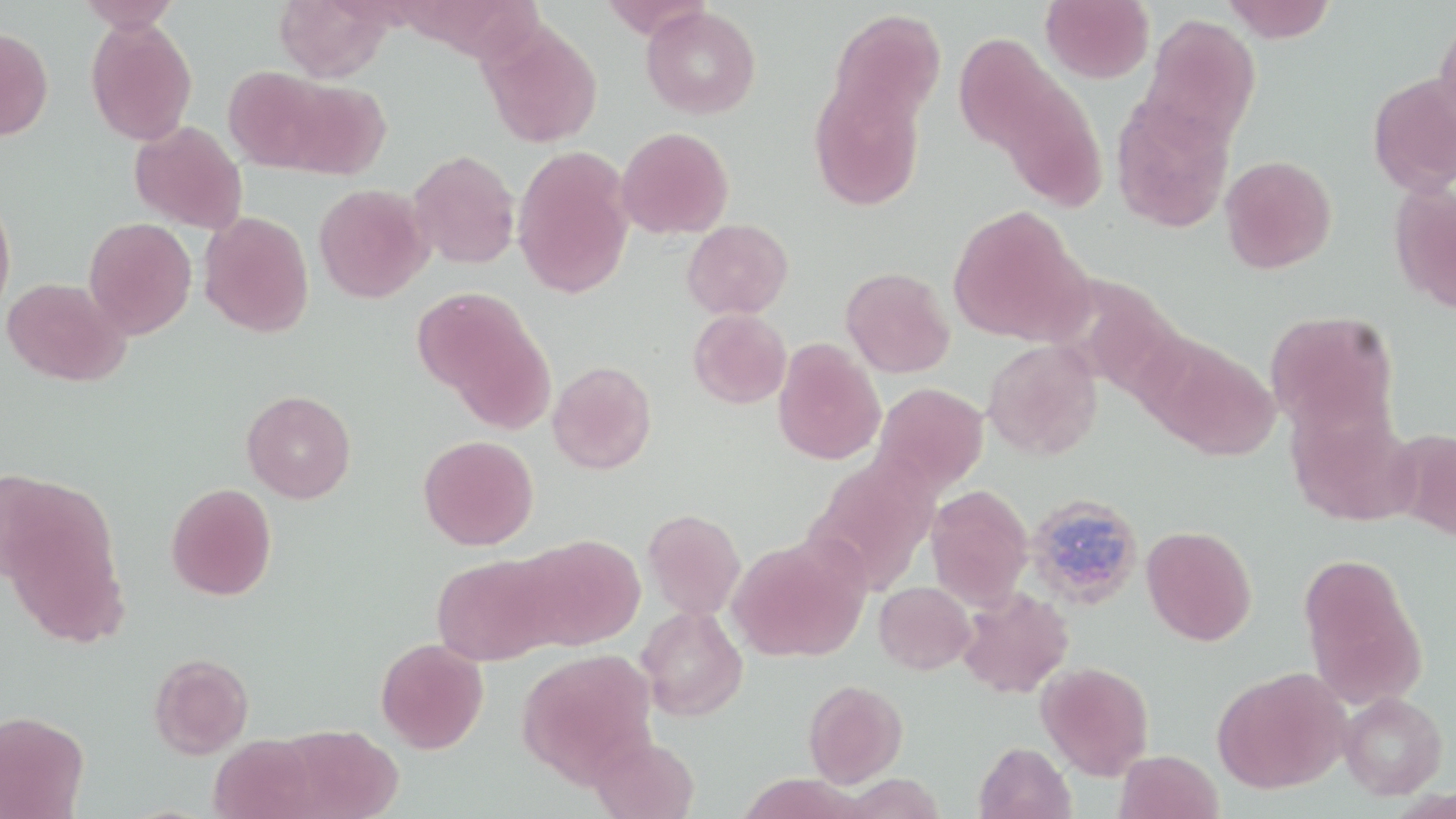
Approximate bounding boxes as [x1, y1, x2, y2] in pixels. Uninfected red blood cell locations: [75, 0, 182, 32], [273, 0, 393, 82], [599, 0, 713, 40], [1041, 0, 1154, 83], [1221, 0, 1336, 42], [640, 6, 761, 119], [829, 10, 947, 127], [1140, 13, 1262, 150], [1434, 15, 1456, 136], [85, 18, 197, 146], [477, 19, 604, 149], [0, 27, 54, 141], [953, 32, 1057, 156], [223, 66, 330, 171], [1367, 73, 1456, 196], [281, 78, 392, 179], [808, 78, 926, 211], [999, 80, 1109, 212], [1110, 94, 1235, 234], [129, 120, 248, 234], [616, 127, 734, 239], [512, 146, 634, 298], [407, 149, 520, 269], [1219, 155, 1337, 274], [1389, 180, 1456, 312], [313, 183, 433, 303], [0, 196, 16, 317], [947, 206, 1088, 345], [199, 210, 315, 338], [84, 217, 197, 339], [682, 219, 793, 319], [841, 266, 955, 378], [2, 277, 129, 386], [1071, 282, 1185, 402], [418, 291, 555, 428], [688, 308, 792, 409], [1265, 310, 1398, 434], [1147, 338, 1279, 460], [982, 339, 1103, 460], [773, 340, 886, 465], [547, 360, 656, 474], [873, 382, 990, 494], [241, 390, 356, 504], [1286, 399, 1416, 526], [1392, 428, 1456, 541], [418, 434, 539, 550], [1, 480, 126, 640], [165, 482, 277, 600], [926, 484, 1033, 610], [642, 508, 746, 620], [1141, 525, 1258, 646], [516, 534, 647, 651], [728, 534, 870, 663], [432, 553, 558, 666], [1300, 554, 1426, 707], [874, 581, 976, 674], [956, 587, 1074, 698], [636, 604, 748, 722], [375, 637, 489, 753], [516, 649, 657, 786], [149, 652, 254, 759], [1036, 661, 1154, 780], [1212, 667, 1349, 794], [803, 679, 908, 788], [1338, 691, 1448, 800], [0, 710, 89, 819], [278, 722, 402, 817], [589, 734, 700, 819], [208, 735, 322, 819], [974, 741, 1076, 819], [1115, 750, 1224, 819]. Plasmodium ovale-infected red blood cell locations: [1022, 491, 1144, 611]. Slide-level diagnosis: Plasmodium ovale. Image is 1456×819 pixels. May-Grünwald-Giemsa-stained preparation. Thin blood film. 1000x magnification. Single field of view. Light microscopy.